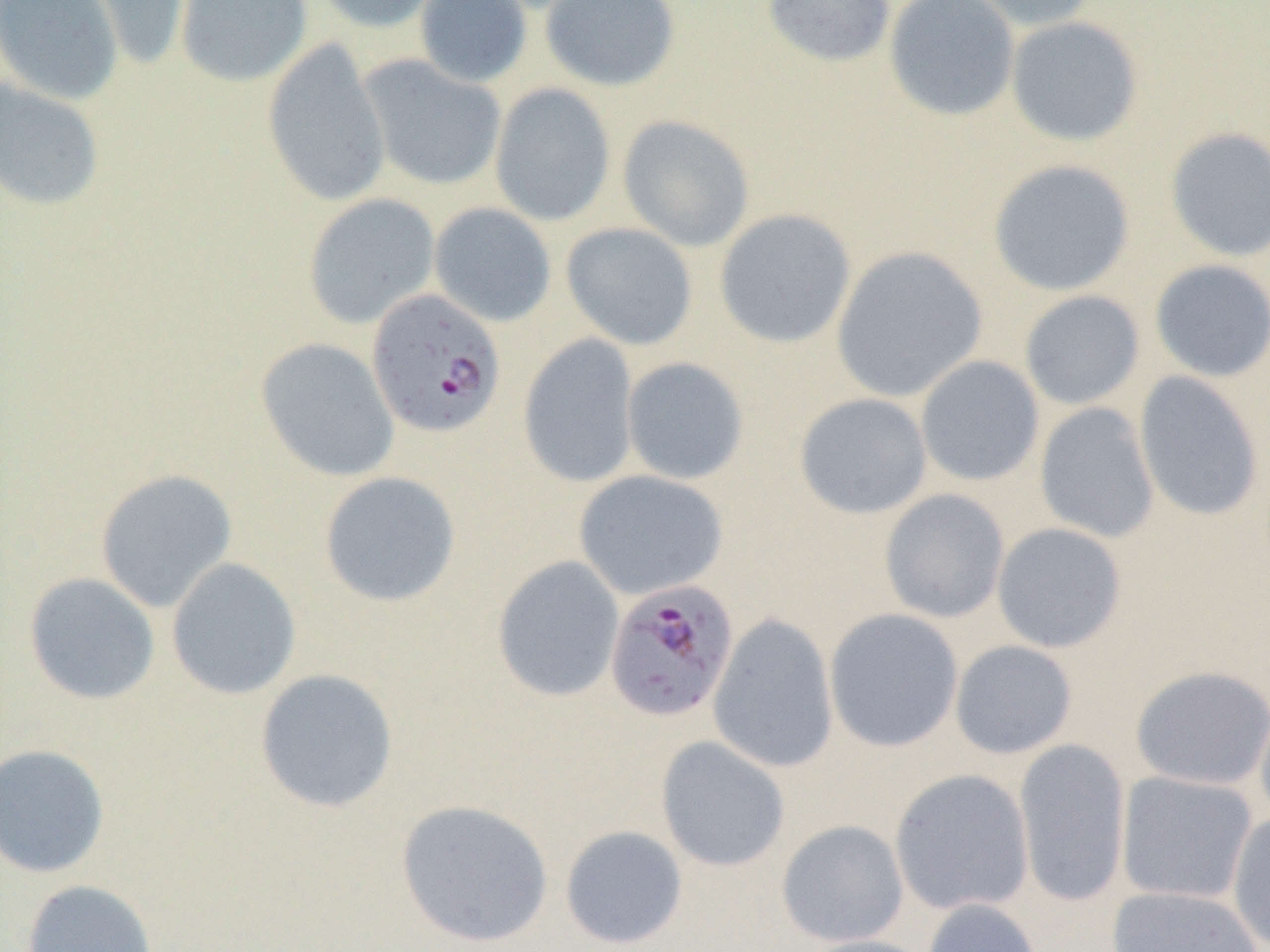
slide-level diagnosis = Plasmodium falciparum
modality = optical microscopy
field of view = one of a larger specimen
preparation = thin blood smear
magnification = 1000x
Plasmodium falciparum-infected red blood cell locations = approximate bounding boxes as named x1/y1/x2/y2 corners in pixels: (x1=367, y1=288, x2=507, y2=438), (x1=611, y1=579, x2=745, y2=723)
image size = 1270×952 pixels
uninfected red blood cell locations = approximate bounding boxes as named x1/y1/x2/y2 corners in pixels: (x1=0, y1=0, x2=124, y2=106), (x1=71, y1=0, x2=194, y2=72), (x1=175, y1=0, x2=312, y2=87), (x1=312, y1=0, x2=446, y2=34), (x1=414, y1=0, x2=533, y2=88), (x1=539, y1=0, x2=681, y2=91), (x1=760, y1=0, x2=897, y2=69), (x1=884, y1=0, x2=1020, y2=122), (x1=960, y1=0, x2=1103, y2=32), (x1=1005, y1=15, x2=1144, y2=147), (x1=261, y1=37, x2=391, y2=208), (x1=359, y1=55, x2=506, y2=191), (x1=1, y1=77, x2=106, y2=211), (x1=489, y1=83, x2=616, y2=226), (x1=618, y1=114, x2=755, y2=252), (x1=1164, y1=127, x2=1270, y2=262), (x1=987, y1=158, x2=1136, y2=297), (x1=302, y1=193, x2=440, y2=329), (x1=429, y1=202, x2=557, y2=327), (x1=714, y1=209, x2=857, y2=349), (x1=561, y1=222, x2=698, y2=351), (x1=831, y1=245, x2=988, y2=402), (x1=1150, y1=259, x2=1270, y2=383), (x1=1019, y1=290, x2=1145, y2=411), (x1=518, y1=333, x2=639, y2=488), (x1=255, y1=337, x2=399, y2=482), (x1=915, y1=356, x2=1045, y2=488), (x1=621, y1=357, x2=749, y2=486), (x1=1134, y1=372, x2=1265, y2=522), (x1=794, y1=392, x2=932, y2=519), (x1=1034, y1=402, x2=1160, y2=543), (x1=94, y1=468, x2=238, y2=612), (x1=573, y1=469, x2=728, y2=600), (x1=318, y1=471, x2=461, y2=608), (x1=879, y1=488, x2=1010, y2=624), (x1=991, y1=522, x2=1127, y2=653), (x1=491, y1=555, x2=625, y2=703), (x1=166, y1=557, x2=301, y2=700), (x1=23, y1=572, x2=160, y2=705), (x1=824, y1=608, x2=963, y2=752), (x1=707, y1=613, x2=839, y2=773), (x1=949, y1=640, x2=1078, y2=760), (x1=1130, y1=664, x2=1270, y2=790), (x1=254, y1=668, x2=399, y2=813), (x1=1255, y1=697, x2=1270, y2=828), (x1=655, y1=736, x2=791, y2=872), (x1=1014, y1=738, x2=1130, y2=907), (x1=0, y1=743, x2=111, y2=878), (x1=890, y1=768, x2=1034, y2=916), (x1=1116, y1=771, x2=1258, y2=905), (x1=395, y1=798, x2=554, y2=948), (x1=1227, y1=810, x2=1270, y2=950), (x1=775, y1=819, x2=909, y2=947), (x1=559, y1=825, x2=688, y2=949), (x1=20, y1=879, x2=159, y2=952), (x1=1107, y1=885, x2=1264, y2=952), (x1=923, y1=898, x2=1042, y2=952), (x1=796, y1=934, x2=938, y2=952)